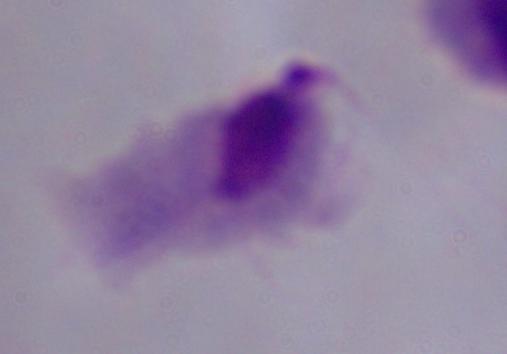
Photomicrograph. 1000x magnification. A trichomonad is shown.